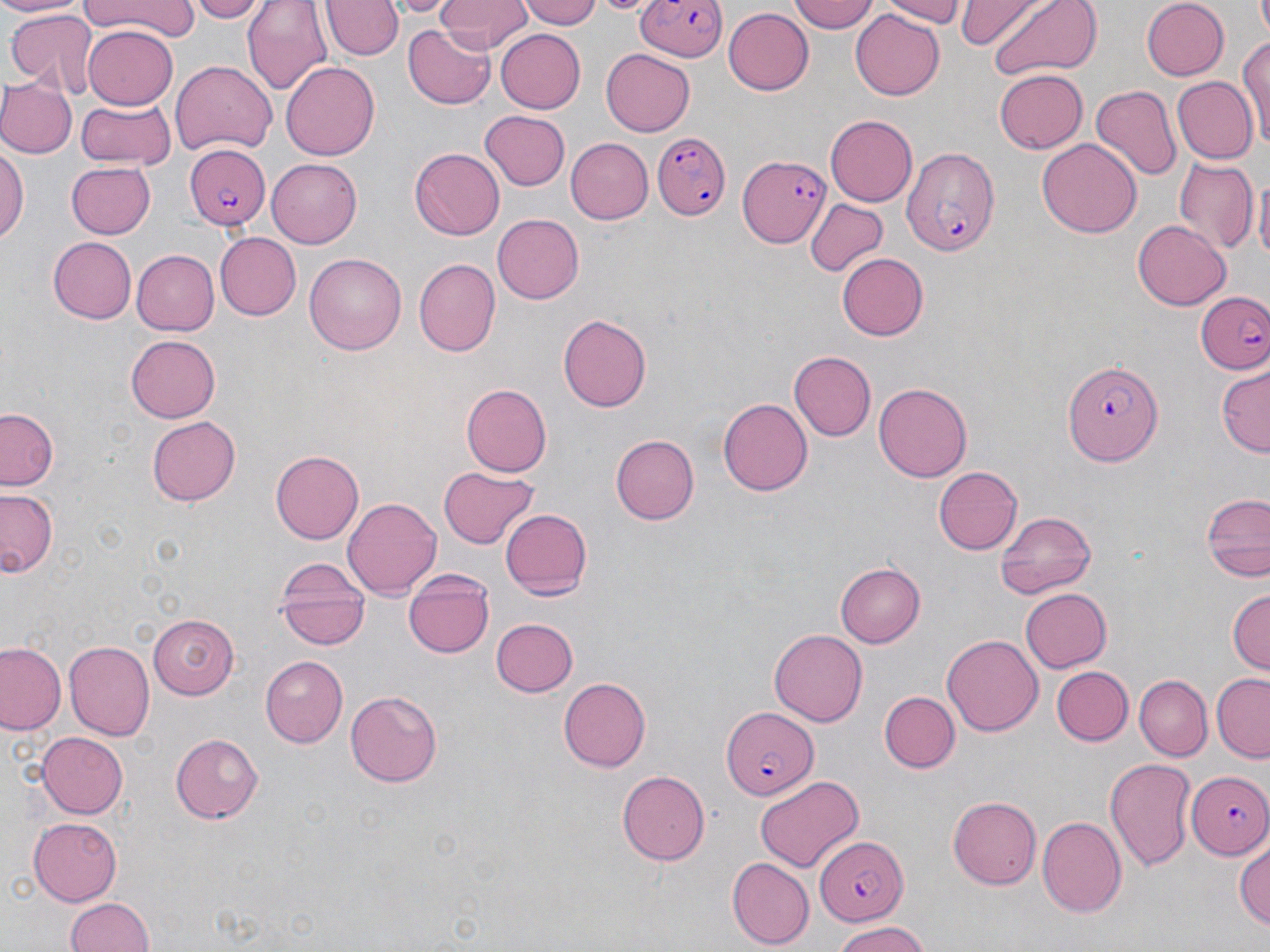

Approximate bounding boxes as named x1/y1/x2/y2 corners in pixels. Plasmodium falciparum-infected red blood cell locations: (x1=637, y1=0, x2=728, y2=63), (x1=654, y1=133, x2=733, y2=220), (x1=897, y1=141, x2=1004, y2=257), (x1=183, y1=143, x2=270, y2=229), (x1=739, y1=156, x2=829, y2=247), (x1=1197, y1=290, x2=1270, y2=373), (x1=1063, y1=360, x2=1164, y2=466), (x1=722, y1=707, x2=818, y2=799), (x1=1185, y1=771, x2=1270, y2=859), (x1=814, y1=836, x2=909, y2=923). Uninfected red blood cell locations: (x1=0, y1=0, x2=82, y2=18), (x1=81, y1=0, x2=196, y2=40), (x1=188, y1=0, x2=268, y2=22), (x1=243, y1=0, x2=334, y2=96), (x1=388, y1=0, x2=456, y2=16), (x1=435, y1=0, x2=532, y2=53), (x1=520, y1=0, x2=607, y2=28), (x1=596, y1=0, x2=652, y2=15), (x1=789, y1=0, x2=877, y2=33), (x1=871, y1=0, x2=965, y2=25), (x1=954, y1=0, x2=1049, y2=46), (x1=985, y1=0, x2=1099, y2=81), (x1=1140, y1=0, x2=1228, y2=79), (x1=323, y1=1, x2=401, y2=61), (x1=6, y1=6, x2=102, y2=97), (x1=723, y1=8, x2=812, y2=95), (x1=850, y1=10, x2=943, y2=100), (x1=83, y1=25, x2=179, y2=110), (x1=403, y1=26, x2=496, y2=108), (x1=492, y1=27, x2=586, y2=114), (x1=1237, y1=34, x2=1270, y2=141), (x1=601, y1=50, x2=695, y2=136), (x1=170, y1=59, x2=277, y2=157), (x1=281, y1=62, x2=379, y2=161), (x1=994, y1=66, x2=1088, y2=152), (x1=1171, y1=76, x2=1257, y2=165), (x1=0, y1=81, x2=76, y2=158), (x1=1091, y1=85, x2=1180, y2=183), (x1=74, y1=97, x2=177, y2=169), (x1=481, y1=110, x2=571, y2=192), (x1=825, y1=116, x2=917, y2=206), (x1=565, y1=137, x2=652, y2=224), (x1=1038, y1=138, x2=1140, y2=239), (x1=0, y1=144, x2=28, y2=248), (x1=410, y1=149, x2=504, y2=240), (x1=1171, y1=155, x2=1256, y2=253), (x1=266, y1=158, x2=363, y2=247), (x1=61, y1=161, x2=156, y2=240), (x1=1253, y1=169, x2=1269, y2=271), (x1=805, y1=198, x2=889, y2=278), (x1=491, y1=212, x2=584, y2=305), (x1=1132, y1=220, x2=1231, y2=310), (x1=215, y1=233, x2=301, y2=320), (x1=46, y1=237, x2=137, y2=324), (x1=133, y1=247, x2=219, y2=335), (x1=304, y1=251, x2=406, y2=352), (x1=835, y1=252, x2=929, y2=342), (x1=412, y1=259, x2=498, y2=358), (x1=558, y1=313, x2=652, y2=411), (x1=126, y1=335, x2=222, y2=423), (x1=788, y1=350, x2=875, y2=440), (x1=1217, y1=365, x2=1269, y2=457), (x1=873, y1=382, x2=972, y2=482), (x1=461, y1=383, x2=552, y2=476), (x1=718, y1=398, x2=813, y2=496), (x1=1, y1=407, x2=62, y2=491), (x1=147, y1=417, x2=240, y2=505), (x1=611, y1=434, x2=699, y2=524), (x1=271, y1=449, x2=367, y2=544), (x1=439, y1=466, x2=541, y2=549), (x1=933, y1=466, x2=1021, y2=553), (x1=1, y1=489, x2=61, y2=580), (x1=1200, y1=490, x2=1269, y2=585), (x1=342, y1=495, x2=440, y2=601), (x1=499, y1=505, x2=592, y2=599), (x1=994, y1=509, x2=1097, y2=597), (x1=277, y1=561, x2=370, y2=649), (x1=837, y1=561, x2=925, y2=647), (x1=403, y1=571, x2=496, y2=659), (x1=1021, y1=588, x2=1114, y2=673), (x1=1226, y1=588, x2=1269, y2=677), (x1=148, y1=614, x2=239, y2=699), (x1=492, y1=616, x2=577, y2=696), (x1=769, y1=628, x2=867, y2=727), (x1=942, y1=633, x2=1041, y2=734), (x1=0, y1=641, x2=66, y2=736), (x1=65, y1=641, x2=154, y2=741), (x1=261, y1=655, x2=349, y2=746), (x1=1050, y1=667, x2=1132, y2=745), (x1=1135, y1=675, x2=1211, y2=760), (x1=1210, y1=675, x2=1270, y2=760), (x1=560, y1=677, x2=653, y2=771), (x1=877, y1=688, x2=959, y2=774), (x1=345, y1=689, x2=443, y2=787), (x1=37, y1=732, x2=128, y2=819), (x1=169, y1=732, x2=264, y2=823), (x1=1104, y1=756, x2=1197, y2=872), (x1=616, y1=768, x2=709, y2=865), (x1=755, y1=776, x2=864, y2=871), (x1=946, y1=795, x2=1040, y2=889), (x1=1038, y1=816, x2=1126, y2=917), (x1=28, y1=818, x2=122, y2=904), (x1=1234, y1=836, x2=1270, y2=934), (x1=726, y1=856, x2=813, y2=948), (x1=65, y1=897, x2=154, y2=952), (x1=834, y1=922, x2=930, y2=951). Slide-level diagnosis: Plasmodium falciparum. 1000x magnification. May-Grünwald-Giemsa-stained preparation. Light microscopy. Thin blood film. Image is 1270×952 pixels. Single field of view.